Identify the parasite.
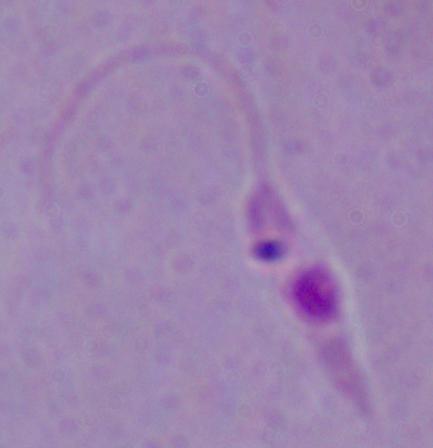

Leishmania.

magnification = 1000x
modality = micrograph